Name the parasite shown.
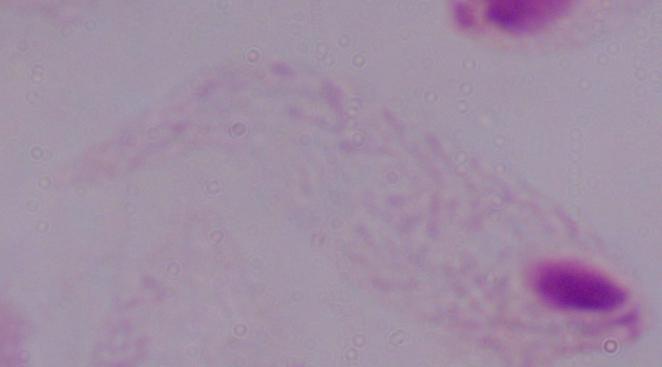
This is a trichomonad.

Summary:
  - Magnification: 1000x
  - Modality: photomicrograph